Assess this cell for malaria.
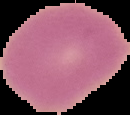
Uninfected.

image size = 130×115 pixels
image type = segmented cell region on a black background
preparation = thin blood film